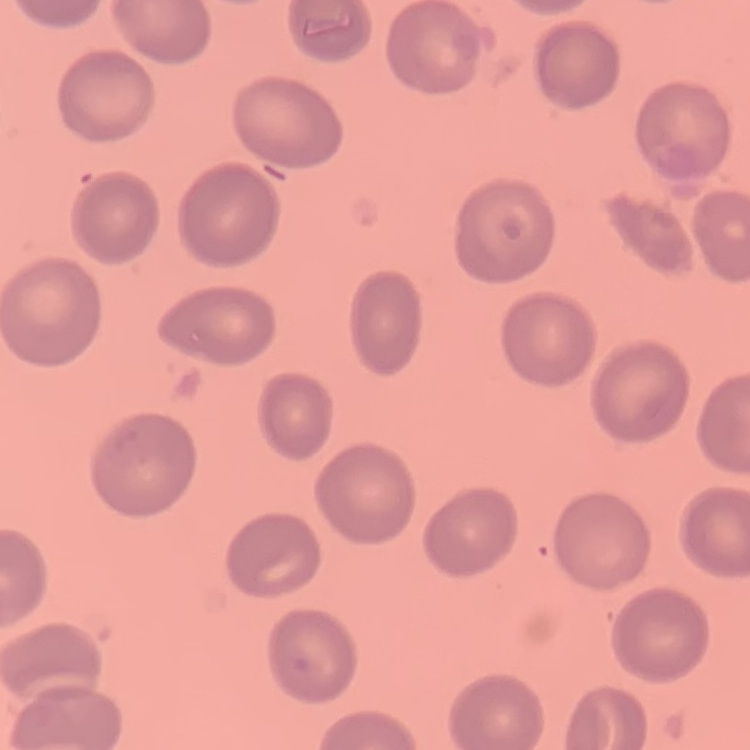
erythrocyte morphology = no rouleaux formation
preparation = thin peripheral smear
stain = Field's or Giemsa
image type = one tile cut from a larger photomicrograph